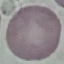
Malaria status: uninfected. Giemsa-stained preparation. Thin smear of blood. Cell patch, automatically extracted from a larger field of view and resized to 64 × 64 pixels. Acquired by smartphone through the microscope eyepiece.